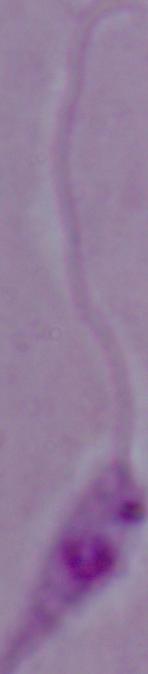
Summary:
  - Modality: photomicrograph
  - Magnification: 1000x
  - Identification: Leishmania